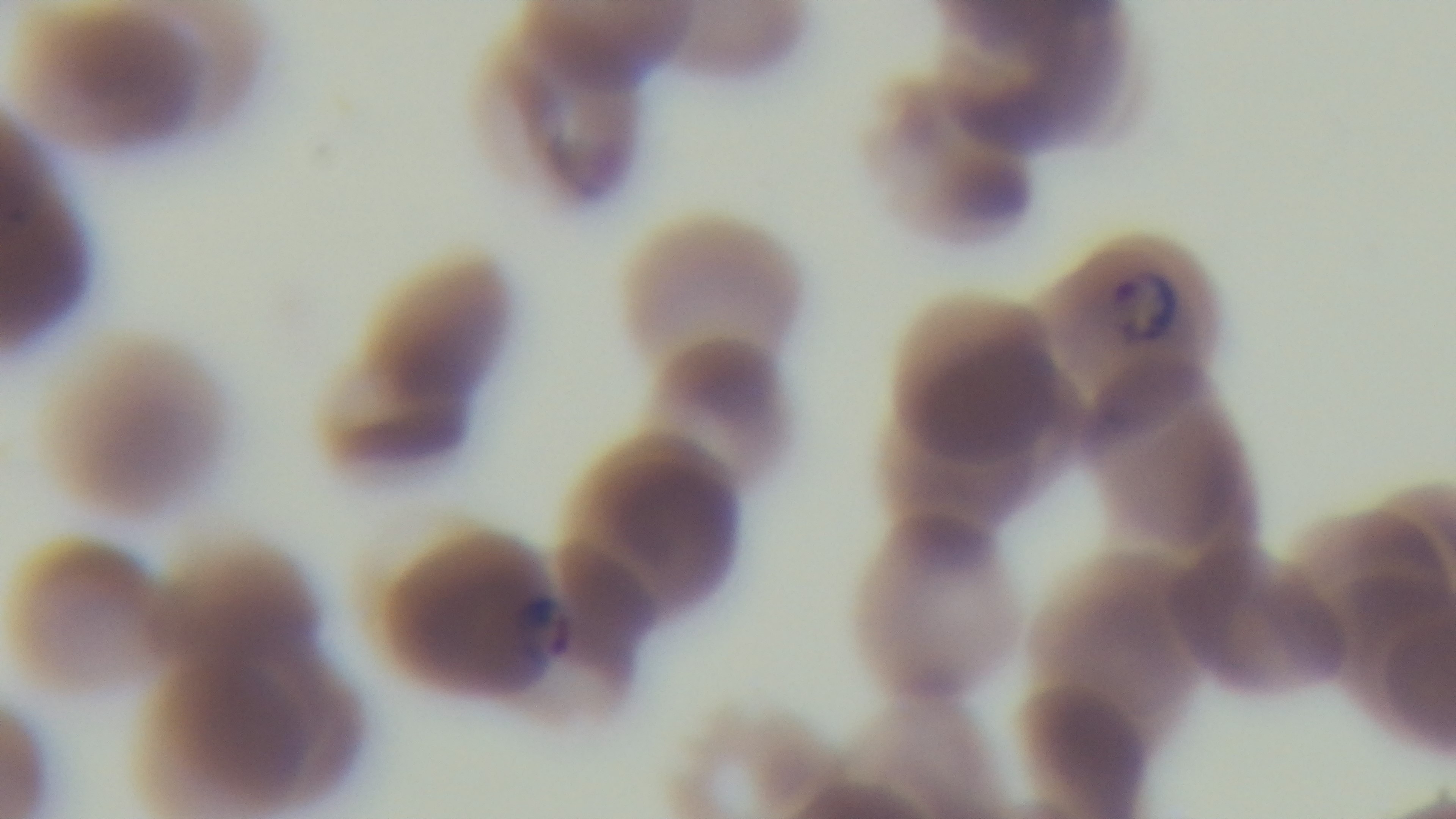
Malaria status: infected. Preparation: thin smear. Photomicrograph. Giemsa stain. Captured with a mounted 4K digital camera. 100x oil-immersion objective. Single field of view.